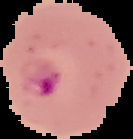

preparation = thin blood smear
result = malaria parasites identified
image type = segmented cell region with the area outside set to black
image size = 133×139 pixels